Assess this cell for malaria.
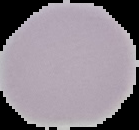

It is uninfected.

image type = segmented cell region on a black background
preparation = thin blood film
image size = 139×130 pixels